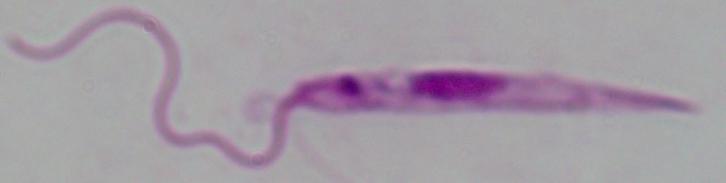
Summary:
  - Modality: micrograph
  - Magnification: 1000x
  - Identification: Leishmania